Outline each blood parasite and name the species.
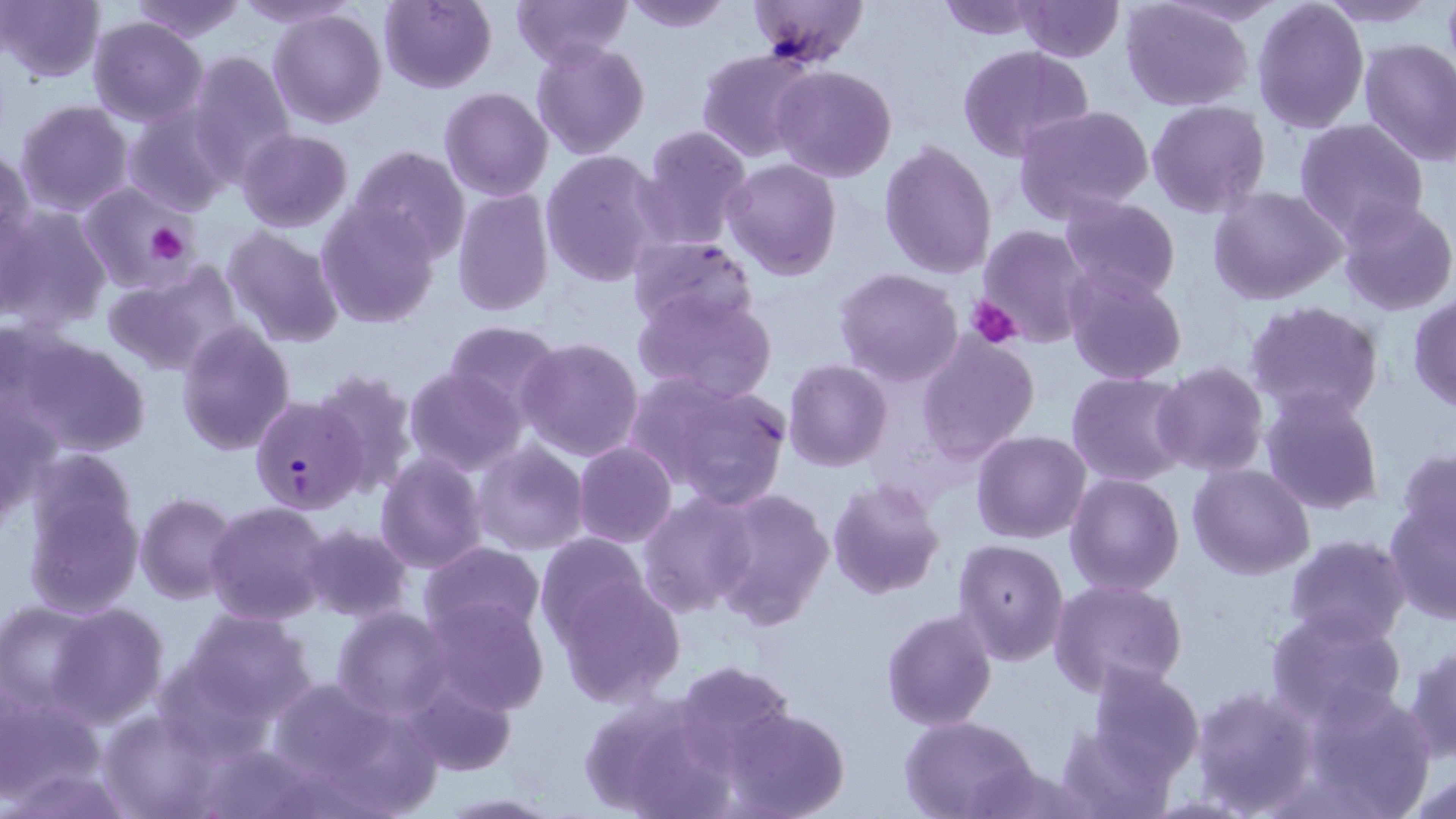

Approximate bounding boxes as (x1, y1, x2, y2) in pixels.
Plasmodium falciparum-infected red blood cells: (249, 395, 367, 514).
No Plasmodium ovale, Plasmodium malariae, Plasmodium vivax, Babesia divergens, or Trypanosoma brucei observed.

Summary:
  - Platelet locations: (143, 220, 194, 265), (968, 295, 1024, 348)
  - Uninfected red blood cell locations: (231, 0, 360, 28), (378, 0, 497, 94), (511, 0, 633, 68), (622, 0, 732, 32), (747, 0, 870, 69), (934, 0, 1050, 39), (1016, 0, 1123, 62), (1315, 0, 1441, 27), (0, 1, 105, 83), (127, 1, 252, 43), (1120, 1, 1254, 110), (1252, 1, 1369, 134), (268, 7, 388, 129), (88, 17, 208, 127), (1357, 37, 1456, 165), (531, 39, 651, 158), (956, 45, 1095, 164), (696, 48, 820, 162), (186, 50, 297, 178), (770, 64, 897, 183), (439, 87, 553, 201), (14, 99, 135, 216), (1147, 101, 1272, 218), (122, 103, 237, 216), (1014, 104, 1154, 223), (1292, 119, 1430, 240), (637, 125, 753, 250), (237, 128, 353, 233), (879, 140, 999, 282), (0, 144, 33, 264), (347, 145, 471, 267), (539, 148, 668, 286), (722, 158, 843, 281), (80, 183, 194, 289), (451, 186, 556, 316), (1207, 186, 1347, 306), (1059, 196, 1182, 304), (1336, 197, 1456, 317), (315, 201, 440, 329), (0, 206, 111, 332), (978, 224, 1094, 347), (221, 226, 344, 348), (627, 235, 758, 332), (102, 262, 243, 378), (834, 268, 963, 387), (1064, 271, 1185, 386), (632, 288, 778, 406), (1408, 294, 1456, 413), (1244, 300, 1386, 422), (444, 321, 562, 420), (176, 322, 297, 457), (12, 331, 152, 459), (916, 334, 1040, 464), (517, 337, 644, 462), (784, 358, 892, 471), (1152, 361, 1270, 478), (311, 367, 422, 497), (403, 368, 524, 472), (1066, 371, 1192, 487), (630, 373, 795, 511), (1260, 387, 1384, 517), (1, 393, 53, 531), (972, 430, 1091, 544), (473, 441, 588, 557), (572, 441, 676, 548), (1396, 449, 1456, 554), (375, 454, 488, 573), (1187, 463, 1316, 581), (1065, 471, 1185, 594), (825, 479, 946, 601), (21, 480, 144, 622), (710, 487, 833, 630), (637, 489, 760, 617), (135, 493, 243, 605), (205, 500, 332, 625), (1382, 500, 1454, 625), (299, 523, 413, 624), (533, 533, 653, 646), (1284, 533, 1411, 645), (953, 538, 1069, 664), (419, 541, 545, 641), (552, 574, 686, 707), (1049, 578, 1189, 697), (423, 596, 549, 715), (47, 600, 170, 726), (2, 601, 104, 714), (332, 605, 453, 719), (1265, 605, 1409, 728), (881, 608, 999, 731), (181, 609, 320, 725), (1404, 639, 1456, 764), (674, 660, 795, 768), (1087, 661, 1207, 780), (403, 677, 516, 778), (265, 679, 434, 810), (1188, 683, 1318, 813), (1301, 685, 1434, 817), (0, 691, 109, 806), (573, 693, 729, 818), (722, 706, 851, 819), (98, 708, 223, 818), (900, 715, 1040, 819), (1055, 725, 1175, 818), (435, 792, 567, 817)
  - Slide-level diagnosis: Plasmodium falciparum
  - Magnification: 1000x
  - Field of view: single
  - Modality: optical microscopy
  - Image size: 1456×819 pixels
  - Preparation: thin blood film
  - Stain: May-Grünwald-Giemsa